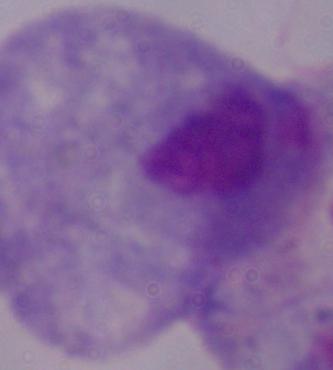

identification: trichomonad
modality: photomicrograph
magnification: 1000x